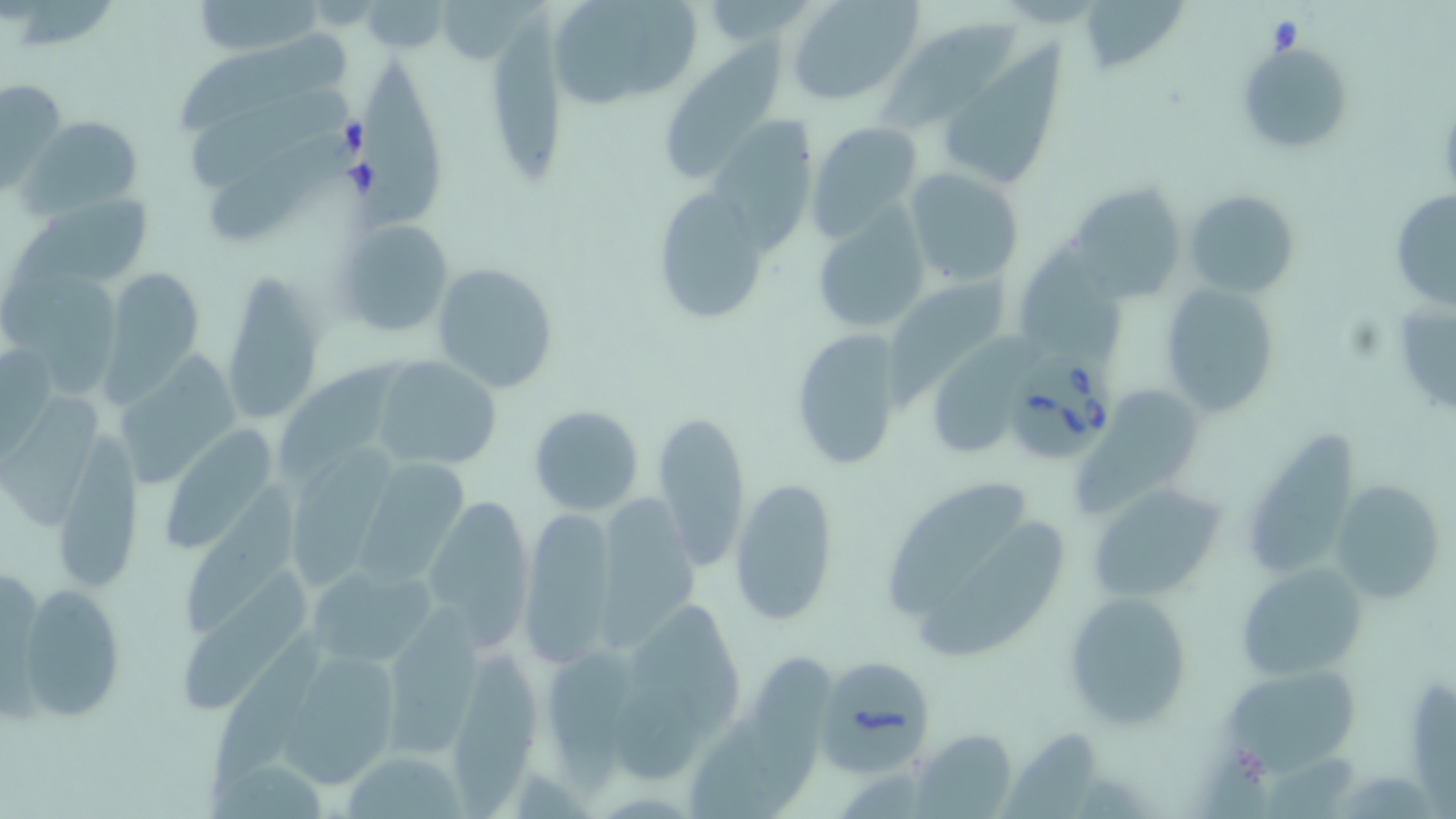

Summary:
  - Coordinate format: approximate bounding boxes as [x1, y1, x2, y2] in pixels
  - Babesia divergens-infected red blood cell locations: [1008, 350, 1116, 457], [817, 657, 933, 772]
  - Uninfected red blood cell locations: [544, 0, 706, 113], [788, 0, 922, 105], [189, 1, 327, 55], [360, 3, 451, 50], [1085, 3, 1187, 80], [489, 11, 567, 186], [885, 19, 1024, 131], [179, 28, 348, 136], [1237, 39, 1353, 155], [660, 40, 791, 182], [935, 48, 1069, 197], [360, 62, 447, 228], [1, 75, 67, 192], [191, 85, 347, 193], [23, 115, 143, 215], [705, 118, 819, 251], [806, 120, 923, 239], [211, 134, 347, 249], [903, 166, 1025, 289], [1068, 183, 1185, 302], [650, 187, 773, 327], [1391, 188, 1456, 311], [1183, 189, 1301, 298], [27, 194, 154, 289], [810, 208, 930, 334], [332, 219, 453, 339], [1017, 239, 1129, 373], [1, 257, 122, 399], [431, 261, 560, 394], [103, 266, 204, 406], [224, 266, 324, 421], [892, 268, 1012, 405], [1159, 282, 1281, 417], [1390, 301, 1455, 416], [789, 327, 905, 472], [930, 333, 1046, 457], [113, 349, 243, 492], [281, 353, 404, 478], [372, 356, 502, 470], [1074, 390, 1208, 517], [7, 393, 101, 526], [528, 404, 644, 515], [653, 409, 750, 568], [166, 424, 271, 551], [64, 428, 145, 588], [1241, 434, 1361, 584], [290, 442, 400, 585], [359, 456, 468, 585], [729, 476, 839, 626], [884, 478, 1029, 617], [1331, 479, 1448, 604], [178, 481, 306, 630], [1088, 484, 1224, 603], [598, 488, 704, 654], [423, 494, 537, 647], [518, 507, 618, 666], [921, 524, 1065, 658], [304, 559, 444, 673], [1235, 563, 1365, 681], [183, 565, 315, 707], [13, 582, 126, 723], [1062, 592, 1195, 731], [630, 596, 748, 735], [389, 599, 489, 763], [209, 632, 330, 799], [451, 642, 534, 819], [289, 647, 397, 787], [549, 649, 651, 794], [747, 651, 836, 812], [1220, 662, 1360, 770], [1409, 676, 1456, 819], [607, 677, 718, 780], [688, 713, 777, 819], [914, 728, 1018, 817], [1000, 732, 1102, 819], [338, 750, 471, 818]
  - Slide-level diagnosis: Babesia divergens
  - Stain: May-Grünwald-Giemsa
  - Modality: light microscopy
  - Field of view: single
  - Image size: 1456×819 pixels
  - Magnification: 1000x
  - Preparation: thin blood film